Locate every leukocyte (white blood cell).
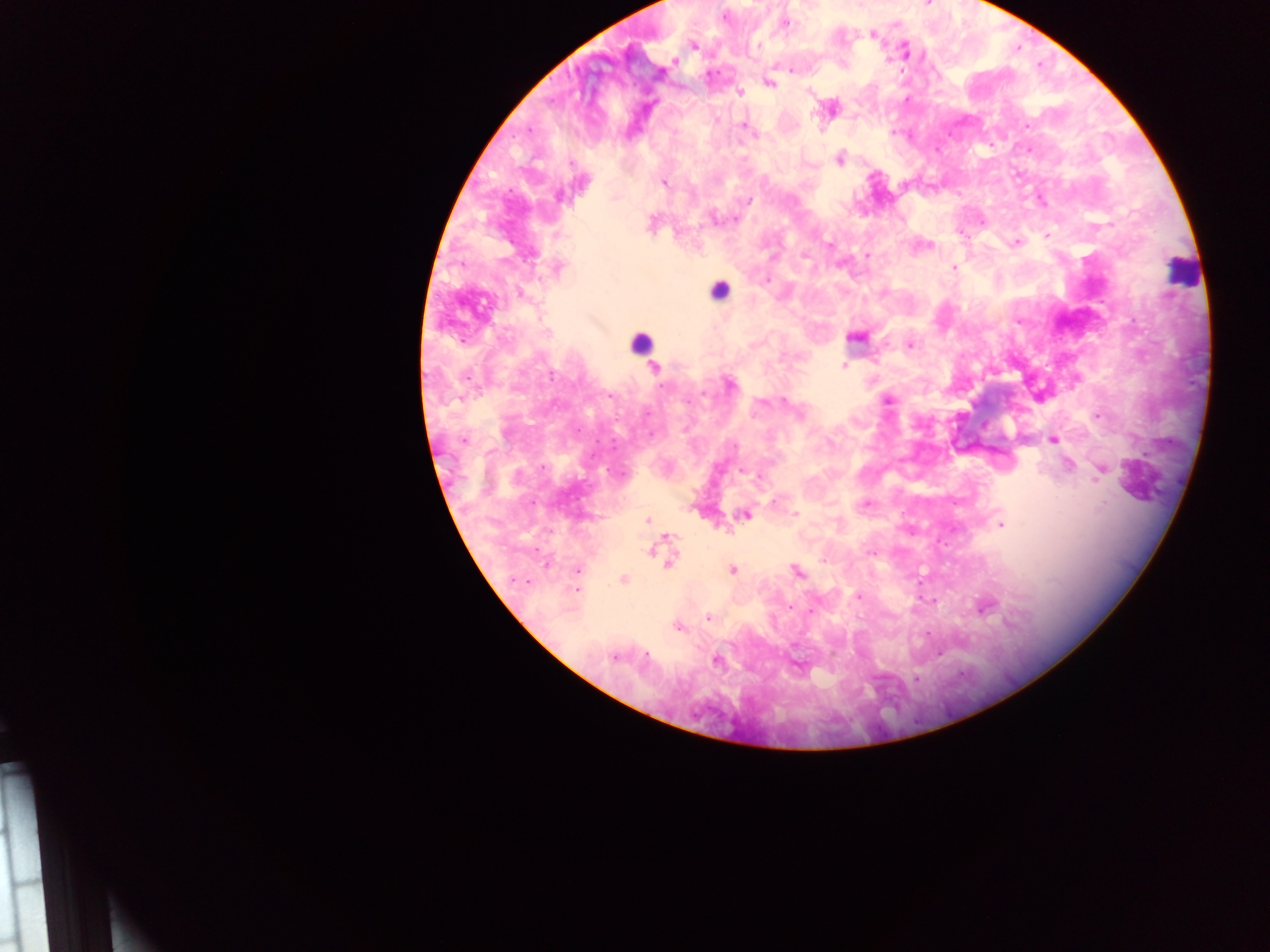
Approximate centers as (x, y) in pixels.
Leukocytes: (1182, 271), (718, 290), (643, 338).

country = Ghana
malaria parasite locations = approximate centers as (x, y) in pixels: (724, 17), (783, 22), (872, 34), (693, 45), (904, 51), (674, 61), (791, 70), (769, 82), (739, 92), (830, 108), (743, 124), (839, 159), (663, 182), (560, 194), (1039, 197), (747, 200), (713, 218), (734, 218), (959, 232), (1046, 236), (1016, 243), (921, 245), (867, 256), (954, 267), (557, 268), (765, 280), (519, 293), (855, 337), (909, 344), (843, 365), (655, 368), (730, 384), (887, 399), (1097, 415), (463, 439), (1052, 439), (1067, 465), (1101, 469), (741, 470), (866, 504), (745, 514), (795, 514), (647, 520), (1000, 524), (661, 548), (666, 557), (576, 570), (731, 570), (796, 571), (623, 579), (526, 581), (577, 589), (859, 596), (934, 599), (983, 606), (789, 607), (708, 618), (677, 627), (646, 653), (938, 653), (614, 655), (716, 660), (916, 678)
image size = 1270×952 pixels
field of view = single
preparation = thick blood film
capture = mobile-phone photograph through a microscope